State which parasite is depicted.
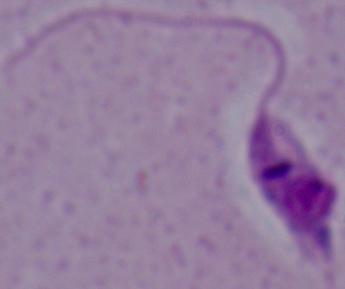
Leishmania.

Photomicrograph. Captured at 1000x magnification.